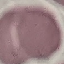
Summary:
  - Malaria status: uninfected
  - Preparation: thin blood smear
  - Stain: Giemsa
  - Image type: cell patch, automatically extracted from a larger field of view and resized to 64 × 64 pixels
  - Capture: smartphone camera at the microscope eyepiece